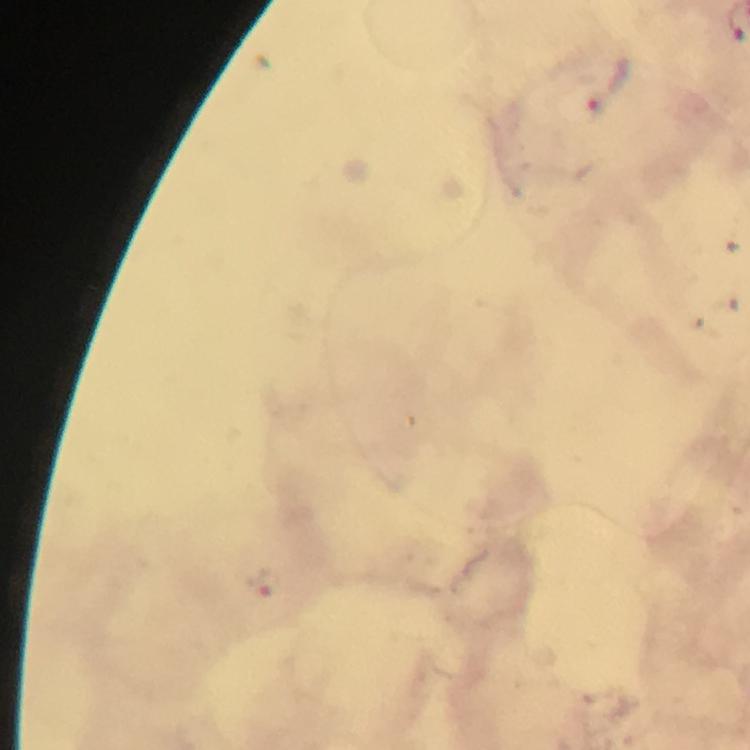

Approximate centers as {x, y} in pixels.
Summary:
  - Malaria parasite locations: {608, 81}
  - Capture: smartphone camera through the microscope
  - Cropped from: one field of view
  - Stain: Giemsa
  - Preparation: thick smear
  - Context: from a malaria diagnostic workup
  - Image size: 750×750 pixels
  - Magnification: 100x
  - Immersion oil: applied